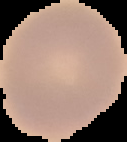

From a thin blood film. Image is 127×142 pixels. Result: no Plasmodium parasites seen. Segmented cell region on a black background.